State the preparation type.
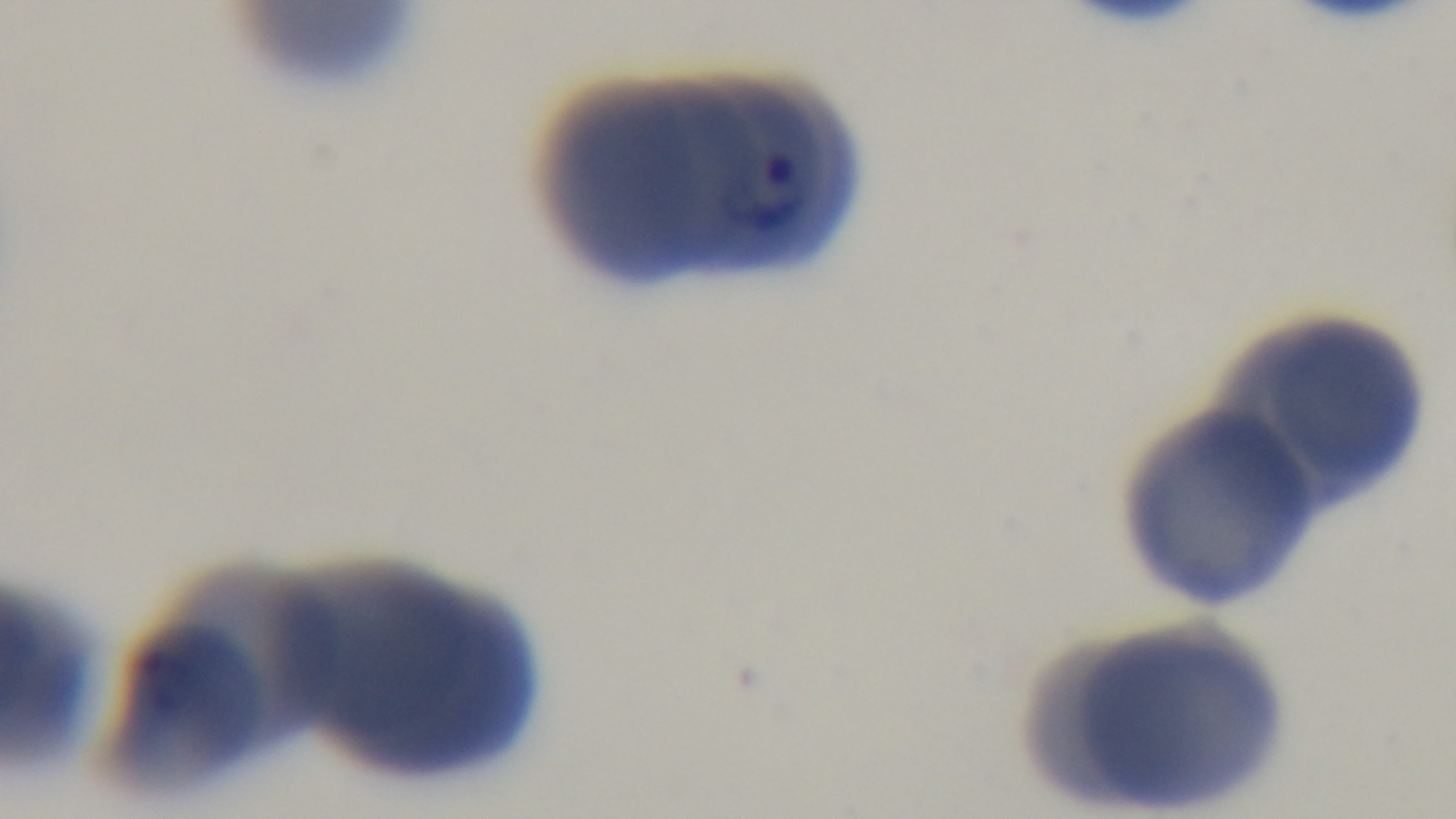
Thin.

Giemsa stain. Single field of view. Light microscopy. Oil-immersion objective, 100x. Mounted 4K digital camera. Malaria status: positive.